State which cell type is depicted.
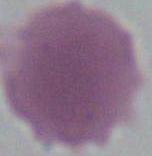

An erythrocyte.

1000x magnification. Micrograph.